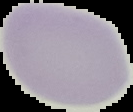

Summary:
  - Result: negative for Plasmodium parasites
  - Preparation: thin blood smear
  - Image size: 133×112 pixels
  - Image type: segmented cell region on a black background